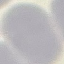
Summary:
  - Result: no malaria parasites seen
  - Preparation: thin blood smear
  - Capture: smartphone through the microscope eyepiece
  - Image type: automatically extracted cell patch, resized to 64 × 64 pixels
  - Stain: Giemsa